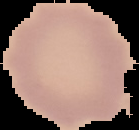
Image is 139×130 pixels. Cell region segmented out of the field of view; the surrounding area is masked to black. Malaria status: uninfected. From a thin blood film.